Locate every blood parasite and identify its species.
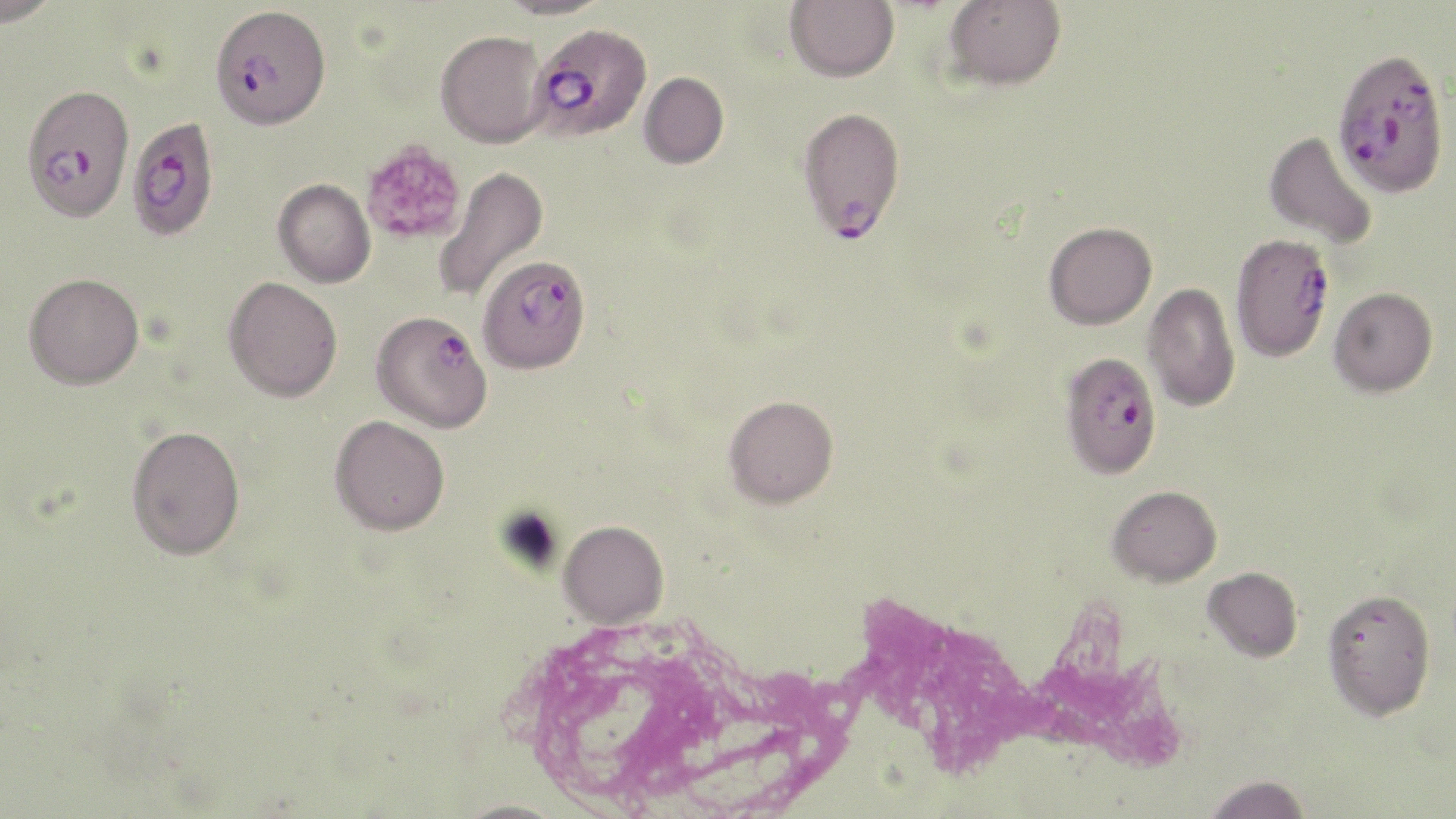
Approximate bounding boxes as (x1, y1, x2, y2) in pixels.
Plasmodium falciparum-infected red blood cells: (209, 5, 331, 130), (529, 22, 652, 142), (1331, 47, 1450, 198), (21, 83, 135, 222), (797, 106, 906, 243), (127, 116, 219, 241), (1225, 239, 1330, 369), (478, 254, 591, 373), (370, 309, 493, 433), (1059, 350, 1162, 479).
No Plasmodium ovale, Plasmodium malariae, Plasmodium vivax, Babesia divergens, or Trypanosoma brucei observed.

{
  "slide_level_diagnosis": "Plasmodium falciparum",
  "magnification": "1000x",
  "white_blood_cell_locations": "approximate bounding boxes as (x1, y1, x2, y2) in pixels: (835, 581, 1195, 793)",
  "preparation": "thin blood smear",
  "uninfected_red_blood_cell_locations": "approximate bounding boxes as (x1, y1, x2, y2) in pixels: (0, 0, 62, 27), (496, 0, 612, 19), (785, 0, 898, 82), (944, 0, 1066, 91), (436, 29, 548, 148), (639, 72, 729, 169), (1264, 130, 1379, 250), (434, 165, 549, 303), (272, 178, 376, 288), (1043, 221, 1157, 330), (24, 273, 144, 389), (223, 276, 343, 402), (1143, 282, 1240, 412), (1329, 287, 1438, 397), (723, 394, 839, 508), (329, 415, 450, 535), (126, 424, 245, 560), (1107, 485, 1222, 587), (559, 520, 669, 628), (1202, 567, 1302, 662), (1322, 588, 1435, 720), (1201, 775, 1312, 818)",
  "image_size": "1456×819 pixels",
  "platelet_locations": "approximate bounding boxes as (x1, y1, x2, y2) in pixels: (360, 139, 467, 246)",
  "stain": "May-Grünwald-Giemsa",
  "modality": "optical microscopy",
  "field_of_view": "one of a larger specimen"
}